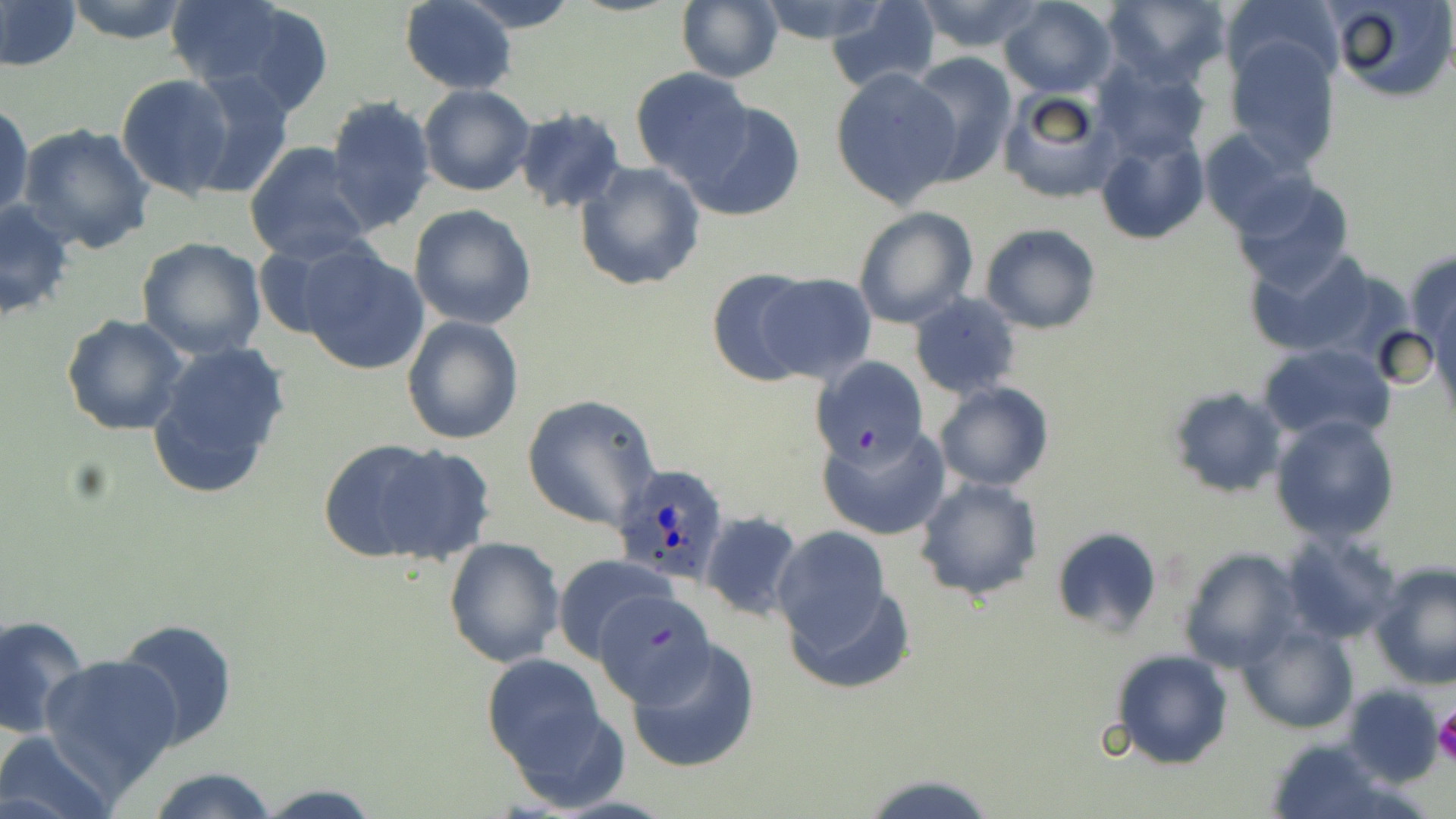
slide-level diagnosis = Plasmodium ovale
stain = May-Grünwald-Giemsa
platelet locations = approximate bounding boxes as (x1, y1, x2, y2) in pixels: (1433, 706, 1456, 766)
uninfected red blood cell locations = approximate bounding boxes as (x1, y1, x2, y2) in pixels: (0, 0, 81, 73), (63, 0, 193, 44), (163, 0, 311, 98), (456, 0, 580, 32), (754, 0, 892, 45), (910, 0, 1046, 52), (999, 0, 1119, 98), (1101, 0, 1231, 87), (1325, 0, 1455, 103), (398, 1, 517, 92), (677, 1, 784, 84), (824, 1, 941, 94), (1222, 2, 1338, 97), (225, 3, 335, 119), (1225, 36, 1340, 168), (906, 54, 1021, 186), (1093, 60, 1209, 160), (830, 68, 962, 208), (630, 69, 754, 182), (183, 71, 297, 197), (116, 73, 236, 198), (419, 85, 535, 198), (998, 87, 1123, 205), (323, 95, 437, 234), (0, 100, 34, 224), (682, 100, 808, 222), (513, 108, 627, 215), (17, 123, 155, 254), (1095, 126, 1209, 245), (1196, 129, 1314, 234), (244, 141, 373, 264), (574, 161, 705, 291), (1228, 174, 1357, 294), (0, 199, 76, 324), (409, 203, 537, 330), (852, 206, 978, 330), (980, 223, 1101, 333), (135, 237, 267, 359), (250, 241, 355, 341), (296, 242, 431, 375), (1245, 248, 1390, 359), (1405, 249, 1456, 355), (705, 267, 821, 386), (754, 274, 878, 384), (910, 293, 1023, 400), (61, 313, 189, 435), (400, 316, 524, 445), (144, 337, 292, 502), (1258, 341, 1395, 443), (814, 357, 926, 464), (934, 382, 1054, 492), (1165, 385, 1290, 498), (521, 393, 661, 531), (1271, 414, 1400, 544), (817, 423, 950, 540), (362, 444, 497, 564), (913, 475, 1043, 604), (699, 510, 804, 621), (770, 527, 892, 649), (1051, 527, 1161, 638), (1279, 531, 1401, 644), (443, 536, 565, 668), (1177, 546, 1301, 671), (552, 554, 674, 662), (1370, 560, 1456, 689), (787, 581, 912, 695), (597, 584, 721, 701), (0, 613, 91, 740), (112, 618, 239, 753), (1238, 622, 1358, 735), (626, 637, 760, 774), (1109, 648, 1234, 769), (39, 654, 183, 790), (482, 654, 609, 775), (1343, 684, 1444, 787), (499, 692, 629, 811), (1, 731, 117, 819), (1265, 739, 1394, 818), (144, 766, 280, 819), (863, 773, 999, 818), (252, 783, 383, 817)
field of view = single
preparation = thin blood film
magnification = 1000x
image size = 1456×819 pixels
Plasmodium ovale-infected red blood cell locations = approximate bounding boxes as (x1, y1, x2, y2) in pixels: (612, 463, 729, 587)
modality = light microscopy